Evaluate for Plasmodium parasites.
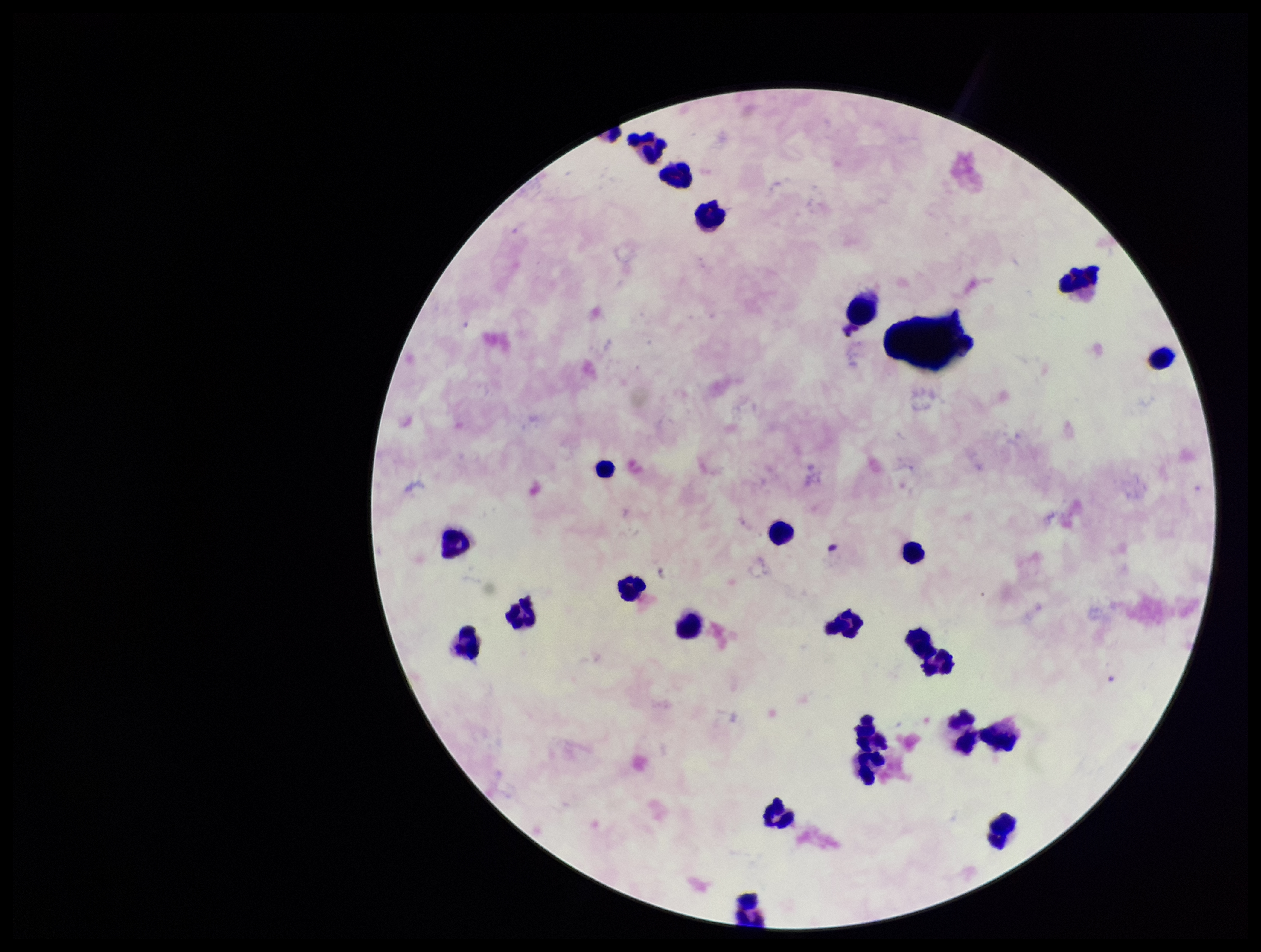

None seen.

Summary:
  - Field of view: single
  - Preparation: thick
  - Image size: 1261×952 pixels
  - Stain: Giemsa
  - Leukocyte count: 25
  - Capture: smartphone photograph through the microscope eyepiece
  - Patient malaria status: negative
  - Parasite count: 0